Describe the morphology of the red blood cells.
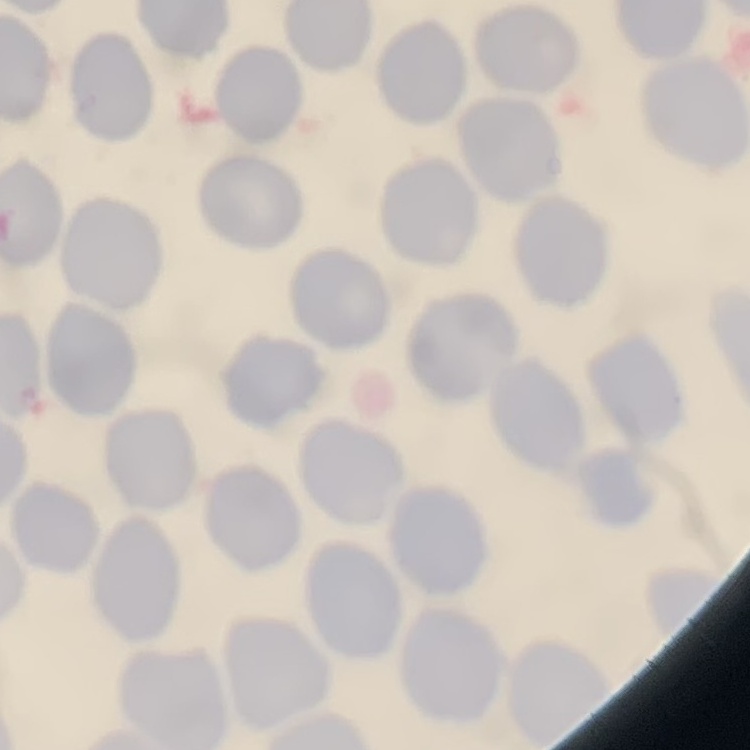
They show no rouleaux formation.

Summary:
  - Preparation: thin blood smear
  - Stain: Field's or Giemsa
  - Image type: one tile cut from a larger photomicrograph